State which parasite is depicted.
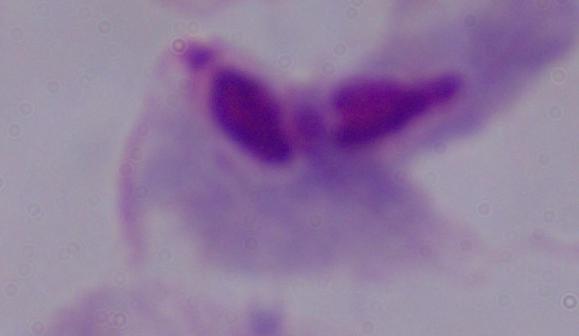
This is a trichomonad.

magnification = 1000x
modality = photomicrograph